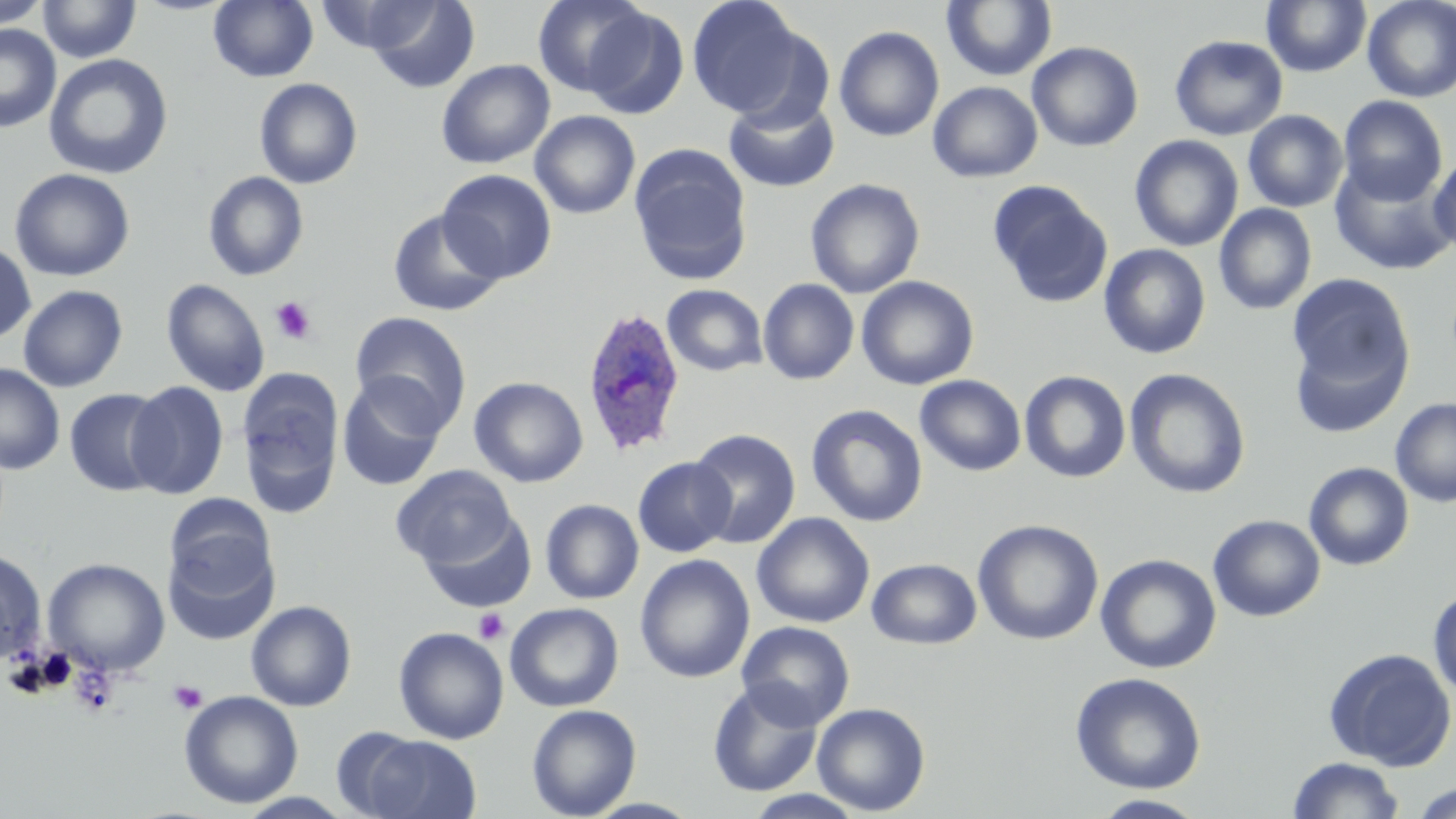
Summary:
  - Coordinate format: approximate bounding boxes as [x1, y1, x2, y2] in pixels
  - Uninfected red blood cell locations: [38, 0, 142, 63], [209, 0, 318, 82], [315, 0, 437, 55], [366, 0, 481, 93], [531, 0, 650, 98], [686, 0, 806, 117], [942, 0, 1057, 81], [1361, 0, 1456, 102], [0, 1, 51, 28], [1261, 1, 1371, 77], [582, 6, 690, 120], [0, 25, 61, 132], [834, 25, 944, 142], [1170, 35, 1288, 140], [1027, 42, 1143, 151], [44, 53, 173, 180], [436, 59, 555, 169], [254, 78, 363, 189], [928, 81, 1043, 183], [1338, 95, 1448, 205], [724, 97, 839, 192], [530, 110, 640, 219], [1243, 110, 1348, 212], [1130, 135, 1243, 252], [629, 144, 753, 286], [1429, 152, 1456, 255], [1330, 162, 1455, 276], [9, 168, 135, 282], [437, 169, 556, 282], [203, 171, 309, 281], [805, 178, 925, 299], [988, 181, 1113, 308], [1213, 204, 1317, 316], [387, 208, 506, 317], [0, 241, 36, 344], [1099, 244, 1211, 359], [1288, 274, 1416, 422], [856, 275, 979, 390], [162, 278, 270, 396], [758, 278, 859, 385], [661, 284, 767, 377], [17, 285, 128, 392], [350, 311, 472, 434], [0, 363, 65, 474], [237, 366, 344, 516], [1125, 368, 1251, 499], [1019, 370, 1131, 483], [337, 375, 447, 491], [915, 375, 1026, 476], [469, 376, 588, 487], [125, 381, 229, 499], [64, 388, 169, 496], [1390, 397, 1456, 508], [806, 405, 928, 527], [689, 429, 800, 549], [632, 456, 736, 558], [1303, 462, 1414, 570], [390, 465, 518, 568], [164, 494, 277, 601], [541, 499, 644, 604], [419, 511, 536, 613], [752, 512, 875, 628], [1208, 515, 1326, 622], [973, 519, 1104, 645], [163, 537, 279, 645], [0, 549, 46, 664], [1095, 553, 1222, 673], [634, 554, 756, 683], [42, 557, 171, 676], [867, 558, 982, 649], [1428, 587, 1456, 702], [246, 600, 357, 711], [505, 602, 624, 712], [736, 621, 855, 729], [393, 626, 509, 744], [1323, 647, 1455, 771], [1070, 671, 1207, 794], [707, 680, 824, 797], [179, 690, 303, 808], [811, 702, 931, 816], [526, 703, 642, 819], [358, 734, 482, 819], [1288, 757, 1404, 818], [1412, 781, 1455, 819], [743, 789, 867, 819], [236, 792, 355, 819], [1091, 794, 1209, 818]
  - Platelet locations: [269, 295, 318, 345], [473, 608, 508, 644], [69, 665, 119, 718], [169, 680, 207, 713]
  - Plasmodium ovale-infected red blood cell locations: [580, 305, 686, 458]
  - Slide-level diagnosis: Plasmodium ovale
  - Stain: May-Grünwald-Giemsa
  - Magnification: 1000x
  - Field of view: single
  - Image size: 1456×819 pixels
  - Preparation: thin blood film
  - Modality: optical microscopy